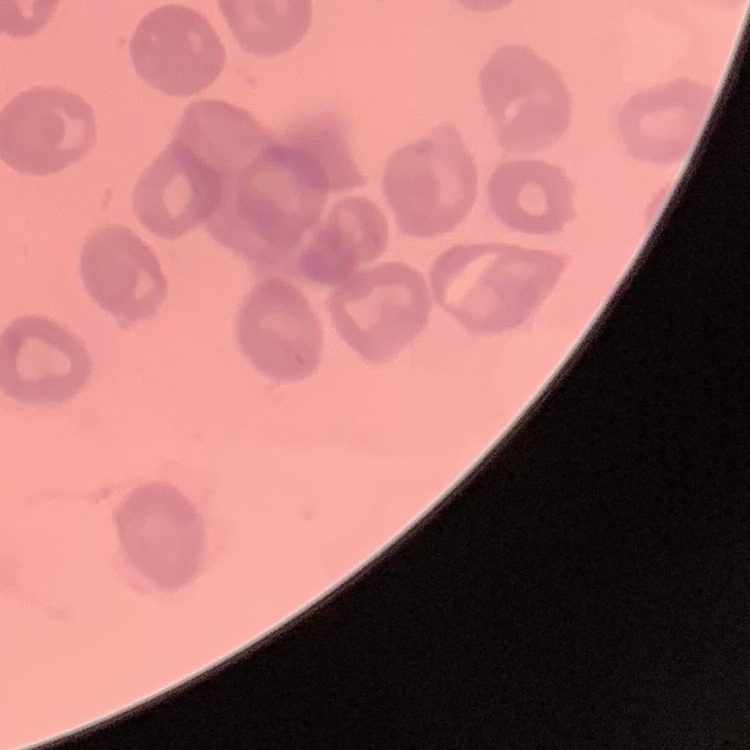
Summary:
  - Erythrocyte morphology: no rouleaux formation
  - Stain: Field's or Giemsa
  - Preparation: thin blood film
  - Image type: one tile cut from a larger photomicrograph